Point out cells.
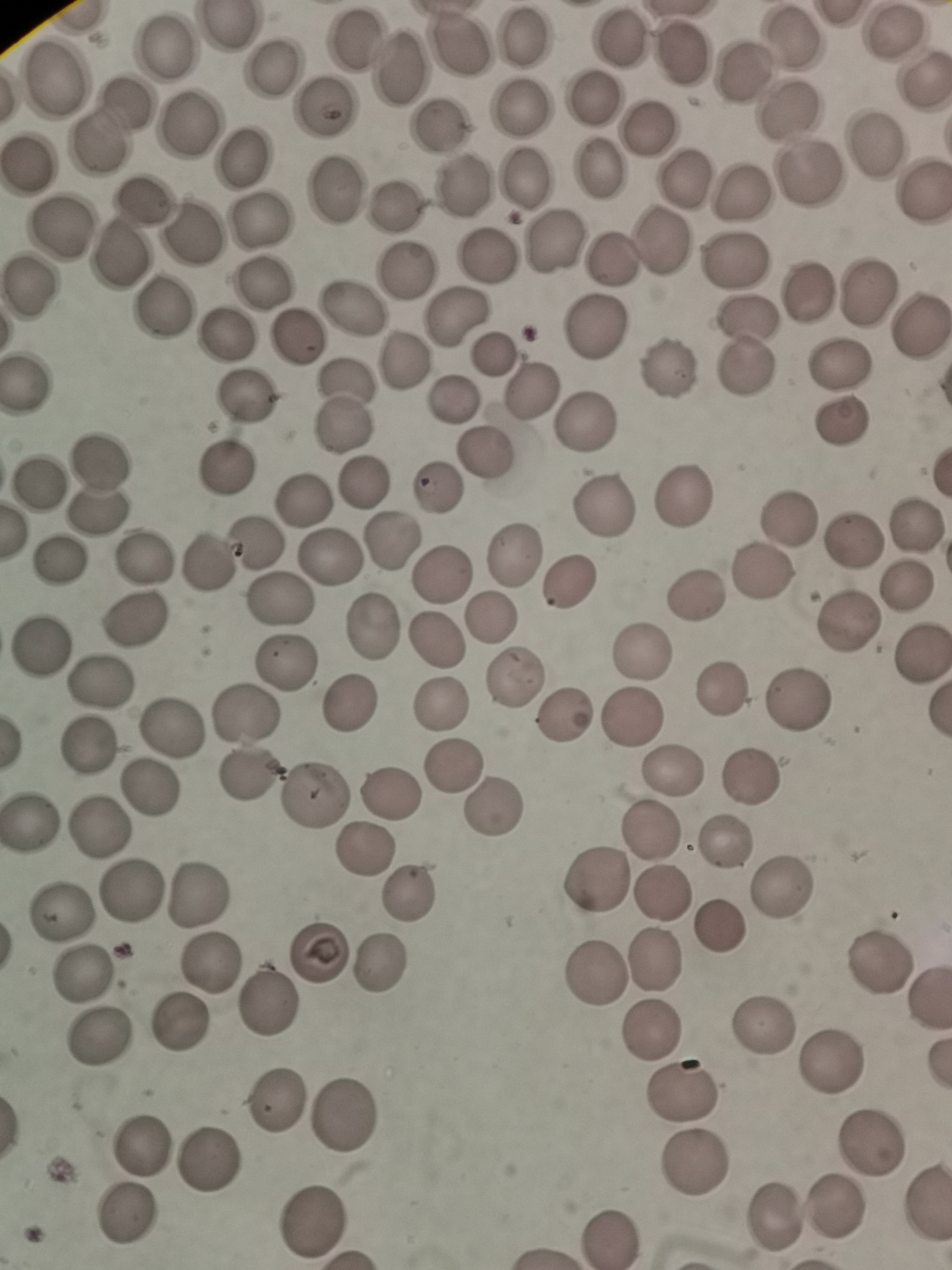

Approximate centers as [x, y] in pixels.
Cells: [226, 26], [527, 37], [459, 40], [356, 43], [163, 46], [268, 70], [395, 74], [53, 76], [591, 96], [327, 103], [125, 104], [519, 108], [188, 124], [441, 129], [100, 141], [246, 156], [29, 164], [594, 169], [524, 176], [338, 186], [463, 189], [140, 197], [396, 204], [261, 220], [61, 225], [191, 235], [551, 240], [661, 241], [115, 254], [485, 254], [737, 260], [607, 261], [408, 270], [264, 283], [29, 287], [807, 289], [864, 292], [160, 307], [352, 307], [455, 317], [745, 321], [596, 329], [915, 329], [297, 335], [228, 336], [495, 354], [401, 361], [838, 364], [671, 368], [742, 369], [28, 378], [530, 392], [248, 395], [453, 403], [344, 404], [837, 421], [585, 422], [486, 452], [100, 460], [224, 466], [40, 479], [365, 481], [436, 491], [686, 493], [304, 499], [607, 504], [96, 513], [786, 522], [917, 525], [854, 538], [392, 542], [257, 543], [514, 554], [332, 555], [57, 556], [207, 560], [144, 561], [442, 575], [762, 576], [569, 584], [909, 584], [698, 595], [279, 599], [490, 618], [136, 620], [846, 620], [373, 628], [435, 639], [42, 646], [643, 649], [921, 649], [285, 665], [512, 678], [102, 681], [723, 686], [798, 700], [349, 703], [441, 706], [564, 714], [246, 715], [631, 719], [172, 723], [88, 744], [451, 765], [673, 771], [248, 775], [748, 780], [148, 786], [390, 795], [313, 797], [491, 809], [31, 823], [650, 829], [97, 830], [726, 839], [362, 849], [593, 881], [129, 889], [414, 891], [778, 892], [657, 893], [198, 897], [61, 913], [716, 926], [319, 948], [654, 961], [876, 961], [209, 963], [381, 963], [84, 976], [596, 976], [928, 991], [265, 1001], [179, 1025], [762, 1025], [650, 1029], [99, 1036], [830, 1061], [684, 1092], [274, 1101], [342, 1116], [872, 1145], [142, 1148], [206, 1159], [690, 1166], [834, 1209], [771, 1213], [123, 1218], [314, 1221].

image size = 952×1270 pixels
field of view = single
preparation = thin blood smear
stain = Giemsa
capture = smartphone through the microscope eyepiece